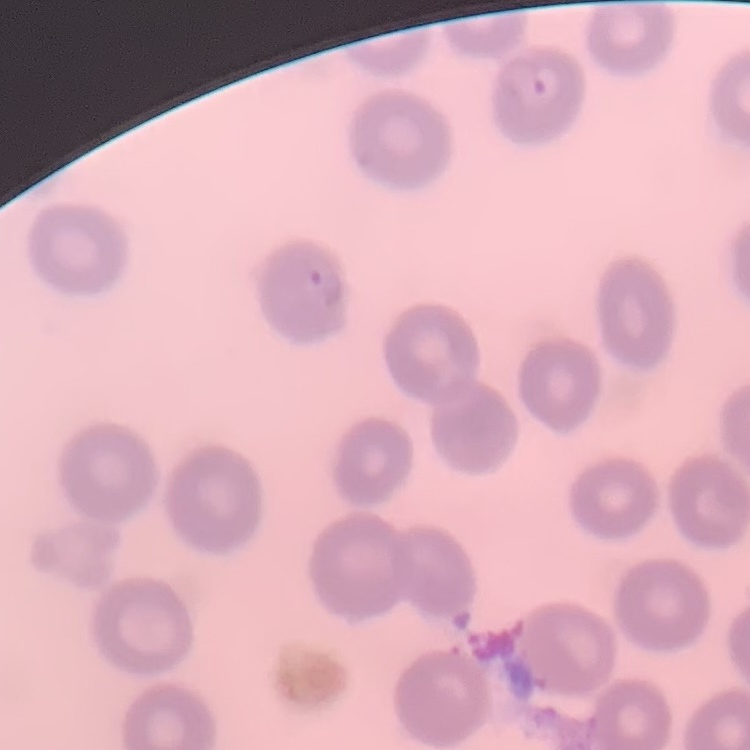 The red blood cells exhibit no rouleaux formation. Square crop of a larger photomicrograph. Thin blood smear. Field's or Giemsa stain.